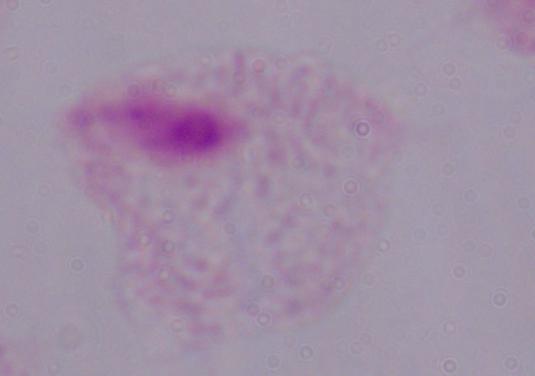

Photomicrograph. A trichomonad is seen. 1000x magnification.